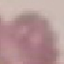

Summary:
  - Malaria status: uninfected
  - Capture: smartphone camera at the microscope eyepiece
  - Preparation: thin blood smear
  - Stain: Giemsa
  - Image type: automatically extracted cell patch, resized to 64 × 64 pixels